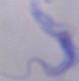
Micrograph. 1000x magnification. A trypanosome is shown.